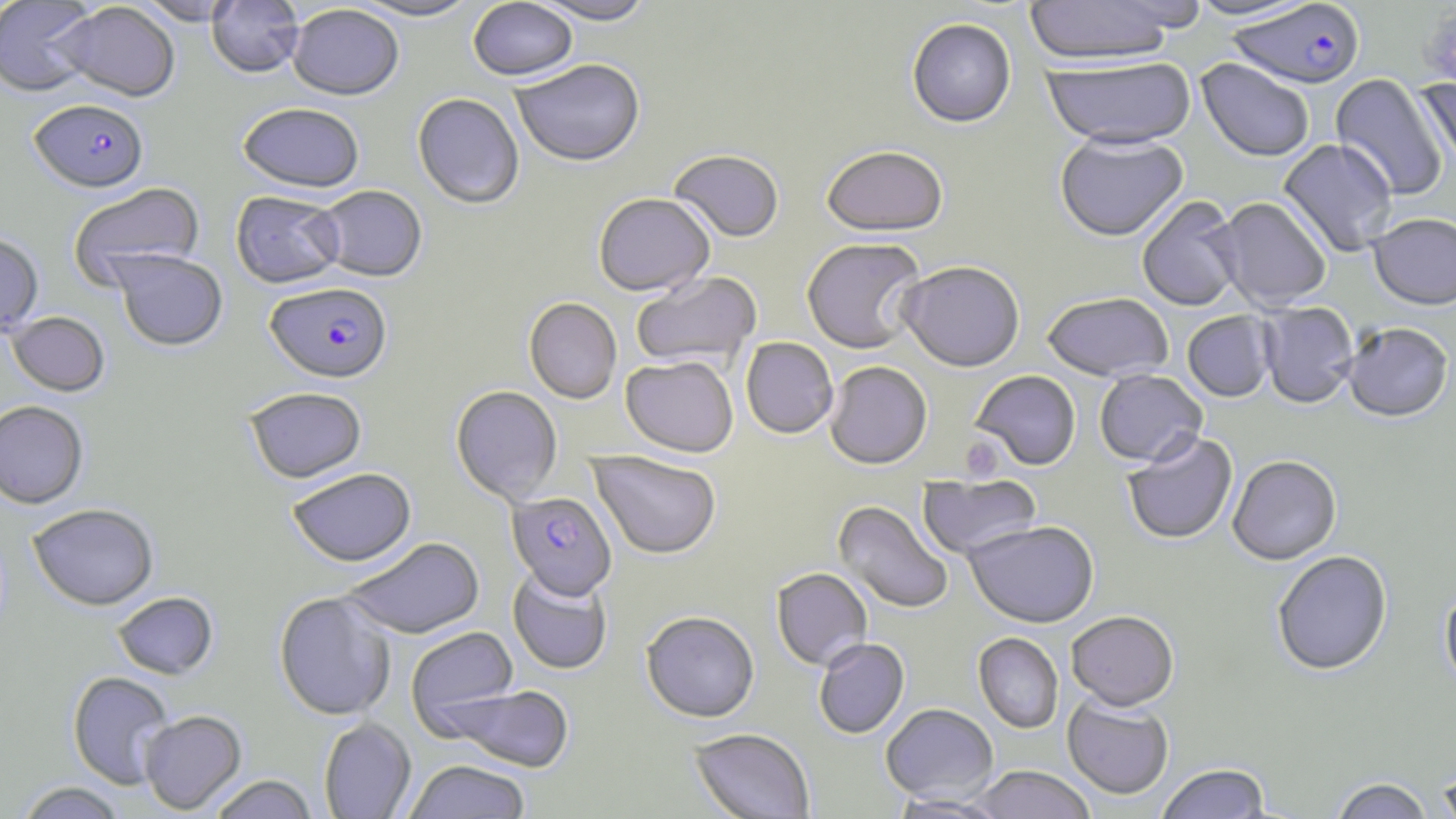
Summary:
  - Coordinate format: approximate bounding boxes as (x1, y1, x2, y2) in pixels
  - Plasmodium falciparum-infected red blood cell locations: (1227, 3, 1364, 92), (29, 99, 149, 194), (265, 283, 392, 384), (507, 492, 616, 600)
  - Uninfected red blood cell locations: (0, 0, 99, 97), (136, 0, 243, 26), (351, 0, 481, 23), (529, 0, 656, 28), (1023, 0, 1183, 71), (1185, 0, 1319, 22), (207, 1, 304, 79), (469, 1, 577, 84), (55, 2, 180, 102), (288, 5, 403, 102), (907, 20, 1016, 130), (1042, 58, 1197, 154), (1195, 60, 1314, 164), (511, 61, 646, 169), (1329, 73, 1449, 200), (1415, 76, 1456, 175), (412, 94, 524, 210), (237, 105, 365, 195), (1055, 134, 1189, 244), (1278, 139, 1398, 258), (822, 149, 948, 241), (668, 152, 784, 244), (68, 182, 205, 289), (316, 186, 427, 283), (231, 191, 345, 289), (593, 195, 715, 299), (1137, 197, 1244, 312), (1211, 198, 1331, 312), (1368, 215, 1456, 314), (0, 234, 43, 339), (802, 240, 926, 355), (112, 250, 227, 352), (897, 263, 1026, 375), (631, 272, 762, 372), (1043, 294, 1173, 384), (524, 298, 622, 405), (1258, 303, 1359, 411), (6, 312, 110, 397), (1183, 312, 1275, 403), (1344, 325, 1454, 425), (740, 338, 838, 440), (620, 357, 737, 459), (825, 363, 933, 471), (1095, 371, 1207, 469), (971, 372, 1081, 472), (244, 386, 368, 484), (451, 386, 563, 505), (0, 401, 89, 509), (1123, 433, 1238, 546), (588, 451, 722, 561), (1228, 457, 1342, 567), (287, 467, 416, 567), (918, 474, 1042, 561), (833, 500, 953, 615), (28, 504, 159, 611), (963, 522, 1100, 630), (340, 537, 485, 639), (1272, 552, 1393, 677), (507, 566, 612, 675), (771, 569, 872, 672), (1440, 587, 1456, 697), (112, 592, 218, 679), (274, 592, 396, 721), (641, 612, 759, 724), (1066, 613, 1179, 714), (406, 626, 519, 735), (973, 633, 1063, 734), (814, 639, 910, 739), (67, 672, 174, 790), (441, 684, 576, 772), (1062, 696, 1174, 801), (881, 704, 998, 804), (139, 710, 246, 814), (319, 717, 416, 819), (689, 729, 815, 819), (404, 760, 531, 819), (1436, 762, 1456, 819), (1156, 765, 1272, 819), (969, 767, 1096, 819), (206, 774, 319, 818), (1330, 778, 1435, 819), (15, 781, 128, 819), (889, 793, 1009, 818)
  - Platelet locations: (1422, 11, 1456, 90), (959, 435, 1004, 482)
  - Slide-level diagnosis: Plasmodium falciparum
  - Field of view: one of a larger specimen
  - Stain: May-Grünwald-Giemsa
  - Magnification: 1000x
  - Preparation: thin blood smear
  - Modality: light microscopy
  - Image size: 1456×819 pixels